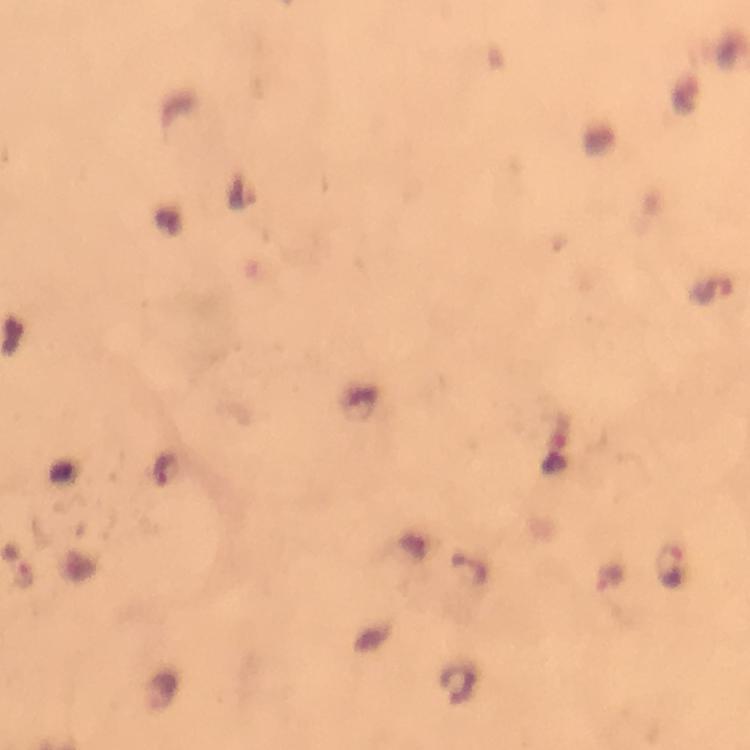 Approximate centers as [x, y] in pixels. Malaria parasite locations: [241, 190], [711, 287], [164, 469], [668, 566], [610, 577]. Image is 750×750 pixels. From a malaria diagnostic workup. Giemsa stain. Photographed with a smartphone mounted on the microscope. Cropped region of a single field of view. At 100x magnification. Thick blood film. Immersion oil was used.